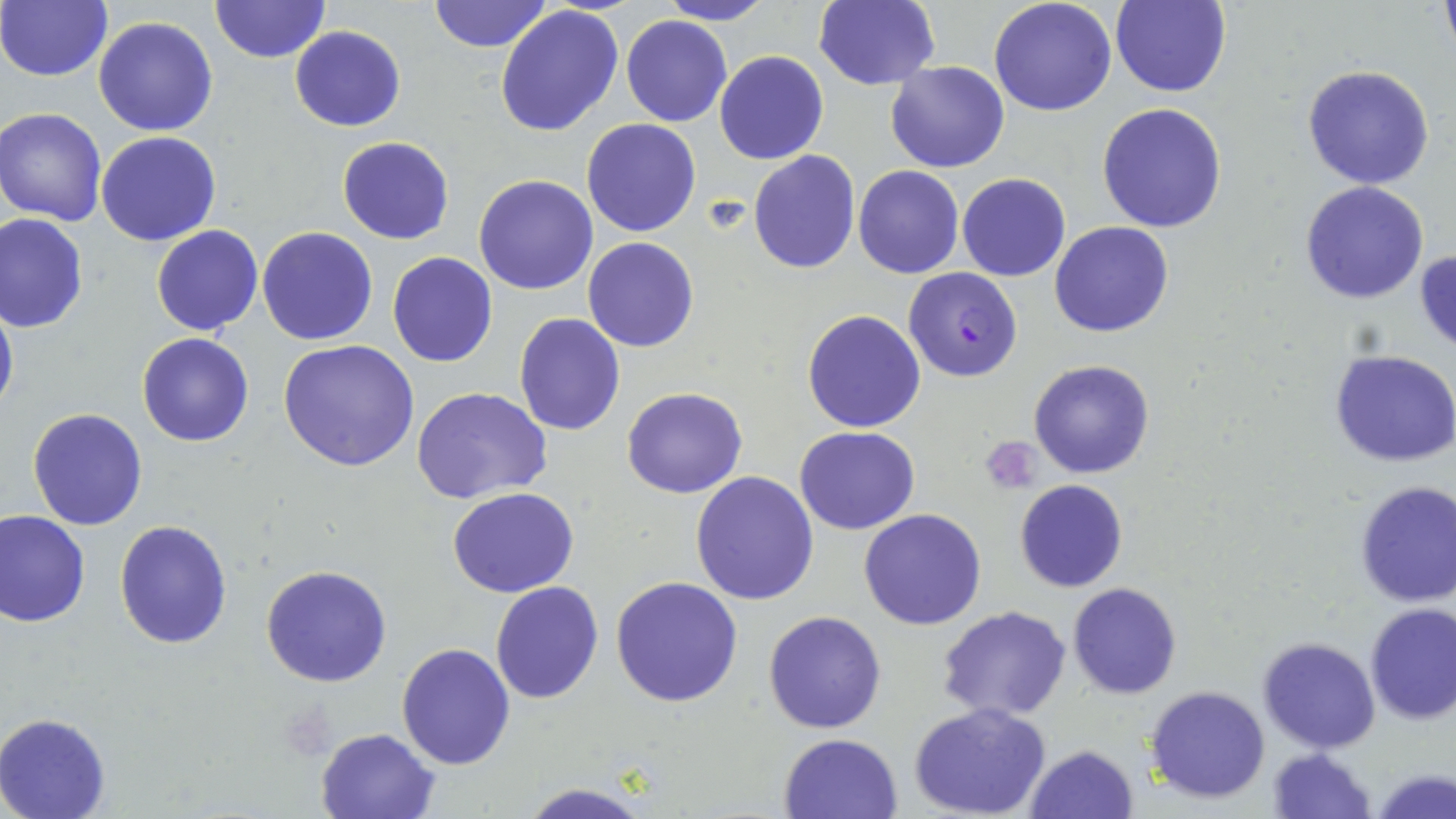
{
  "slide_level_diagnosis": "Plasmodium falciparum",
  "platelet_locations": "approximate bounding boxes as (x1,y1)-(x2,y2) corner pairs in pixels: (700,193)-(750,235)",
  "field_of_view": "one of a larger specimen",
  "uninfected_red_blood_cell_locations": "approximate bounding boxes as (x1,y1)-(x2,y2) corner pairs in pixels: (210,0)-(331,64), (426,0)-(553,52), (813,0)-(940,90), (0,1)-(112,82), (656,1)-(775,25), (988,1)-(1118,117), (1112,1)-(1232,98), (494,5)-(623,139), (621,14)-(732,127), (93,16)-(218,137), (289,26)-(405,132), (715,50)-(828,165), (886,61)-(1009,173), (1303,63)-(1435,190), (1096,102)-(1228,233), (2,107)-(109,224), (582,118)-(703,237), (95,130)-(220,245), (337,137)-(454,245), (748,149)-(861,274), (852,166)-(964,279), (957,173)-(1070,281), (474,174)-(598,294), (1300,181)-(1430,304), (1,213)-(88,331), (1050,220)-(1174,338), (151,224)-(263,335), (257,226)-(379,346), (583,237)-(700,352), (1415,250)-(1456,356), (387,251)-(497,366), (0,293)-(18,421), (802,309)-(926,432), (514,312)-(625,436), (136,332)-(254,447), (278,339)-(420,472), (1330,349)-(1456,466), (1028,360)-(1155,478), (411,387)-(553,504), (622,387)-(746,498), (27,408)-(147,531), (794,426)-(920,536), (690,472)-(820,606), (1014,479)-(1128,593), (1352,481)-(1456,609), (447,486)-(580,598), (0,509)-(91,627), (859,509)-(986,629), (114,519)-(232,649), (260,564)-(392,687), (612,576)-(744,707), (489,580)-(604,704), (1067,583)-(1181,699), (1363,602)-(1456,726), (937,606)-(1072,721), (762,609)-(888,734), (1294,619)-(1451,739), (1258,635)-(1380,753), (396,642)-(517,770), (1145,685)-(1272,803), (909,703)-(1052,819), (0,713)-(111,818), (315,726)-(440,818), (778,732)-(904,819), (1025,742)-(1140,818), (1266,747)-(1378,819), (1373,768)-(1454,819), (513,781)-(661,819)",
  "stain": "May-Grünwald-Giemsa",
  "preparation": "thin blood film",
  "image_size": "1456×819 pixels",
  "modality": "optical microscopy",
  "magnification": "1000x",
  "plasmodium_falciparum_infected_red_blood_cell_locations": "approximate bounding boxes as (x1,y1)-(x2,y2) corner pairs in pixels: (903,267)-(1022,381)"
}